Comment on the morphology of the erythrocytes.
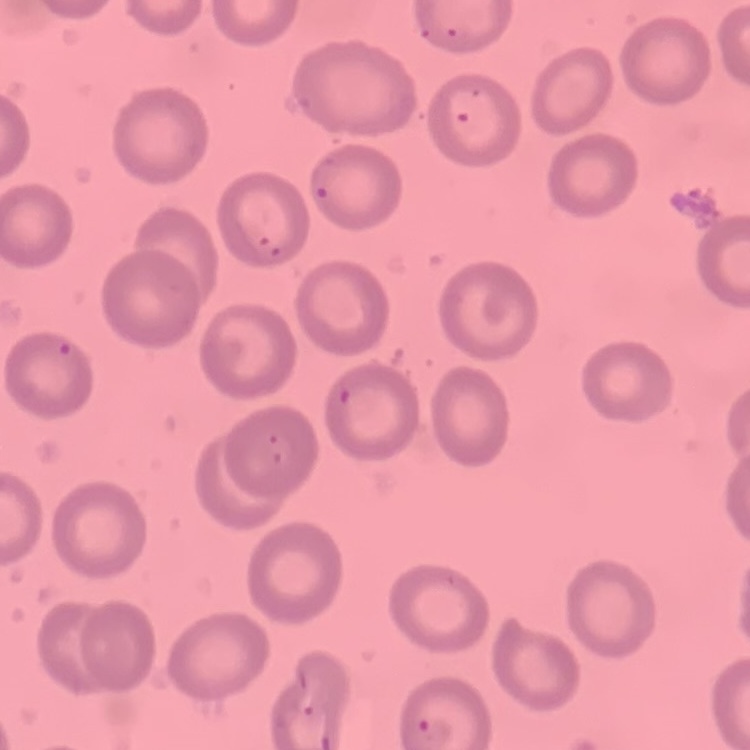

They show no rouleaux formation.

Summary:
  - Image type: one tile cut from a larger photomicrograph
  - Stain: Field's or Giemsa
  - Preparation: thin peripheral smear